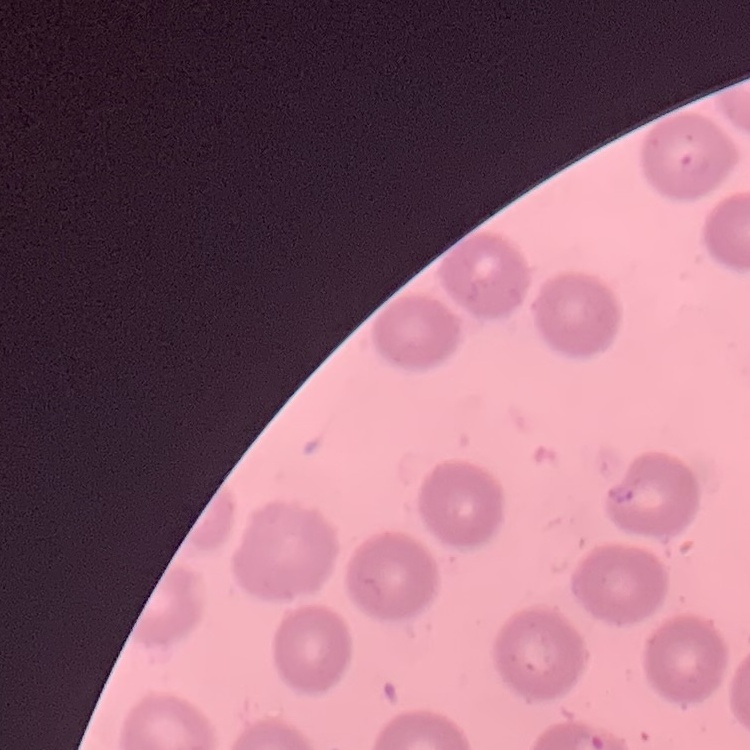
erythrocyte_morphology: no rouleaux formation
image_type: one tile cut from a larger photomicrograph
stain: Field's or Giemsa
preparation: thin peripheral smear